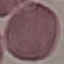

malaria_status: uninfected
image_type: automatically extracted cell patch, resized to 64 × 64 pixels
stain: Giemsa
preparation: thin blood smear
capture: smartphone through the microscope eyepiece